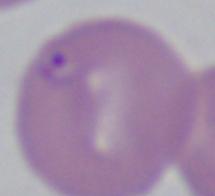

magnification = 1000x
identification = Babesia
modality = photomicrograph